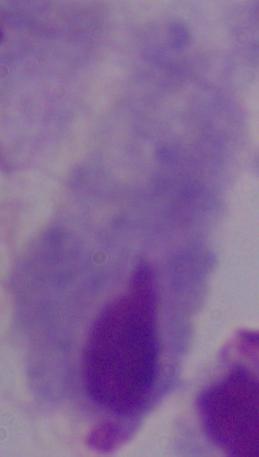
Summary:
  - Magnification: 1000x
  - Modality: micrograph
  - Identification: trichomonad